Identify the blood parasite species.
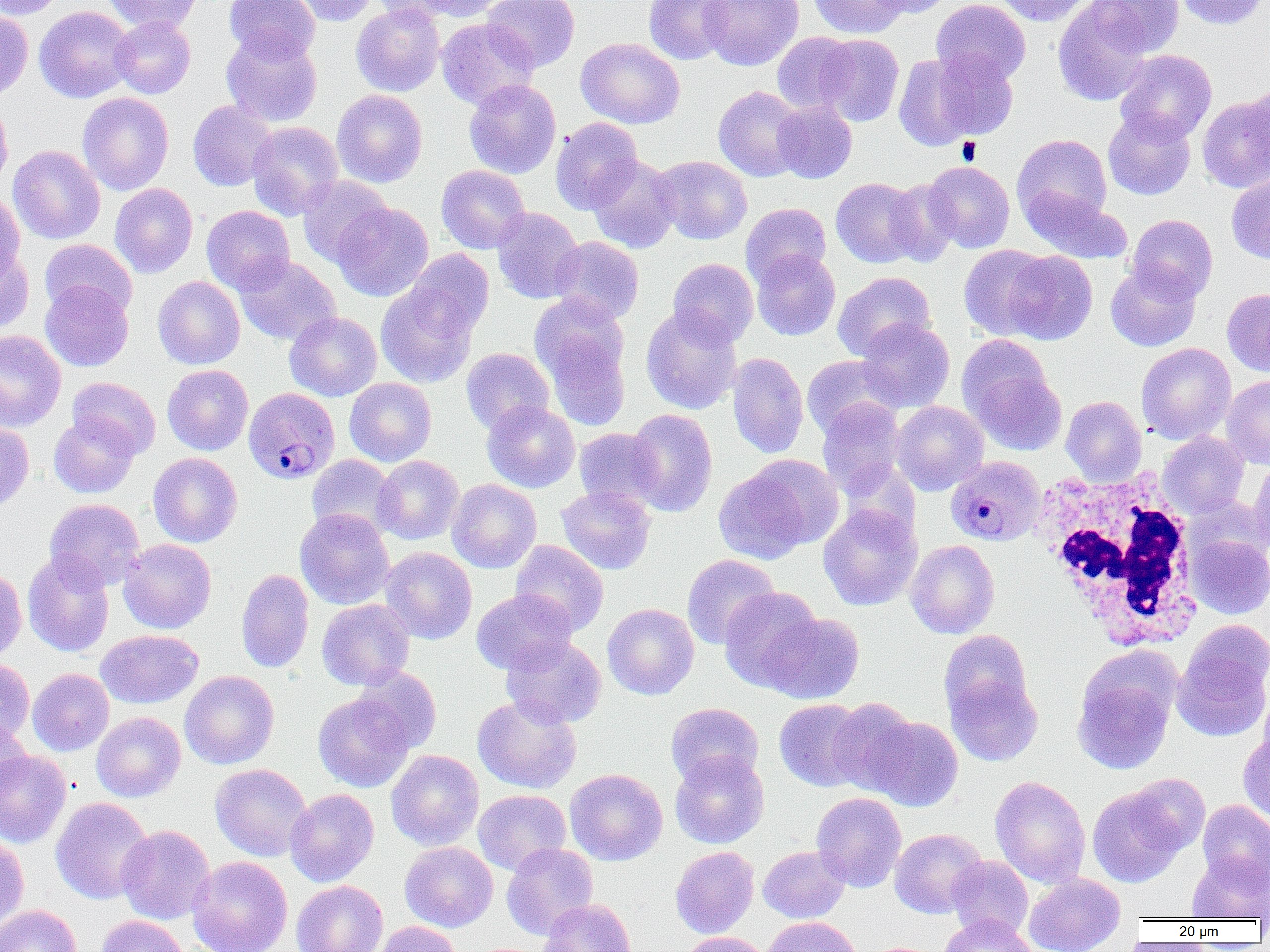

Plasmodium malariae.

Approximate bounding boxes as (x1,y1)-(x2,y2) corner pairs in pixels. Platelet locations: (957,137)-(981,164). White blood cell locations: (1033,468)-(1203,650). Plasmodium malariae-infected red blood cell locations: (248,387)-(345,484), (945,455)-(1046,547). Uninfected red blood cell locations: (0,0)-(65,20), (102,0)-(201,34), (224,0)-(320,63), (288,0)-(379,26), (371,0)-(467,24), (405,0)-(508,21), (482,0)-(580,73), (644,0)-(733,64), (699,0)-(803,71), (808,0)-(908,38), (866,0)-(954,18), (931,0)-(1031,87), (992,0)-(1093,26), (1089,0)-(1184,57), (1174,0)-(1269,29), (1053,1)-(1152,106), (351,2)-(445,96), (34,6)-(136,103), (0,9)-(33,101), (110,16)-(195,98), (436,18)-(539,110), (221,32)-(322,127), (772,32)-(859,114), (817,34)-(904,126), (576,38)-(685,129), (1115,49)-(1217,143), (924,51)-(1021,143), (894,52)-(983,151), (463,79)-(561,179), (1245,83)-(1270,170), (713,86)-(807,181), (332,89)-(427,188), (77,92)-(174,196), (1197,94)-(1270,193), (0,97)-(13,192), (188,100)-(278,191), (772,100)-(857,183), (1103,109)-(1196,200), (550,117)-(643,214), (247,121)-(344,220), (1012,134)-(1113,228), (8,145)-(105,244), (586,155)-(681,253), (651,155)-(752,245), (923,161)-(1015,253), (436,164)-(530,254), (1226,174)-(1270,264), (297,176)-(394,267), (831,178)-(922,268), (885,179)-(961,266), (109,183)-(198,278), (1021,187)-(1133,264), (0,192)-(25,281), (333,203)-(433,301), (741,203)-(831,287), (201,205)-(295,295), (492,207)-(584,303), (1126,214)-(1218,302), (549,236)-(645,325), (39,239)-(137,319), (959,245)-(1057,340), (0,247)-(35,332), (405,249)-(494,338), (751,250)-(841,341), (1002,250)-(1098,344), (234,255)-(341,346), (668,257)-(759,346), (1105,262)-(1201,351), (833,271)-(935,361), (152,276)-(245,370), (40,280)-(134,372), (376,282)-(479,388), (1222,288)-(1270,377), (531,298)-(631,421), (641,305)-(742,414), (284,311)-(382,401), (856,318)-(955,412), (0,330)-(66,431), (958,334)-(1054,423), (1136,342)-(1236,444), (461,348)-(554,435), (727,352)-(809,458), (801,355)-(901,439), (162,365)-(253,455), (969,367)-(1067,455), (1221,375)-(1270,469), (67,377)-(160,459), (344,377)-(437,466), (1061,396)-(1146,485), (817,399)-(907,497), (482,400)-(580,493), (892,401)-(988,495), (626,408)-(718,516), (49,414)-(140,499), (0,422)-(34,512), (574,428)-(665,512), (1158,432)-(1249,518), (148,452)-(242,547), (306,454)-(402,541), (373,455)-(464,545), (1248,457)-(1270,553), (713,461)-(829,562), (447,479)-(542,573), (555,486)-(656,575), (44,498)-(145,589), (818,503)-(922,610), (295,508)-(395,610), (1185,532)-(1270,619), (118,539)-(216,634), (511,540)-(608,637), (906,540)-(1000,638), (380,547)-(477,644), (22,550)-(114,657), (681,554)-(781,649), (0,568)-(27,660), (236,568)-(314,673), (719,586)-(824,692), (471,590)-(577,675), (317,599)-(415,690), (601,603)-(699,699), (764,613)-(865,704), (95,629)-(203,709), (938,630)-(1032,719), (1172,630)-(1270,742), (500,635)-(606,729), (0,659)-(34,744), (352,667)-(442,754), (27,668)-(114,756), (180,670)-(279,769), (1073,670)-(1177,775), (945,671)-(1043,766), (1258,682)-(1270,768), (313,692)-(414,792), (472,694)-(582,793), (827,698)-(922,796), (774,699)-(871,792), (666,702)-(763,788), (91,712)-(186,802), (865,716)-(964,811), (0,719)-(31,801), (1238,733)-(1270,824), (386,749)-(484,850), (0,750)-(72,848), (670,752)-(769,849), (210,763)-(312,861), (565,768)-(668,865), (1124,773)-(1210,854), (990,776)-(1091,887), (1087,784)-(1190,887), (285,788)-(379,887), (473,789)-(571,875), (811,792)-(907,892), (50,796)-(154,905), (1198,800)-(1270,888), (116,825)-(215,924), (890,828)-(987,919), (0,833)-(29,931), (400,842)-(498,932), (501,843)-(598,940), (758,845)-(850,923), (670,846)-(759,938), (1187,853)-(1270,921), (188,856)-(293,952), (946,856)-(1034,940), (1024,873)-(1125,952), (291,879)-(388,952), (539,898)-(636,952), (0,905)-(81,952), (939,914)-(1036,952), (95,915)-(190,952), (762,916)-(864,952), (372,920)-(462,952), (677,932)-(772,952). Light microscopy. One field of a larger specimen. Thin blood smear. Image is 1270×952 pixels. Captured at 1000x magnification.